Give the extent of all uninfected red blood cells.
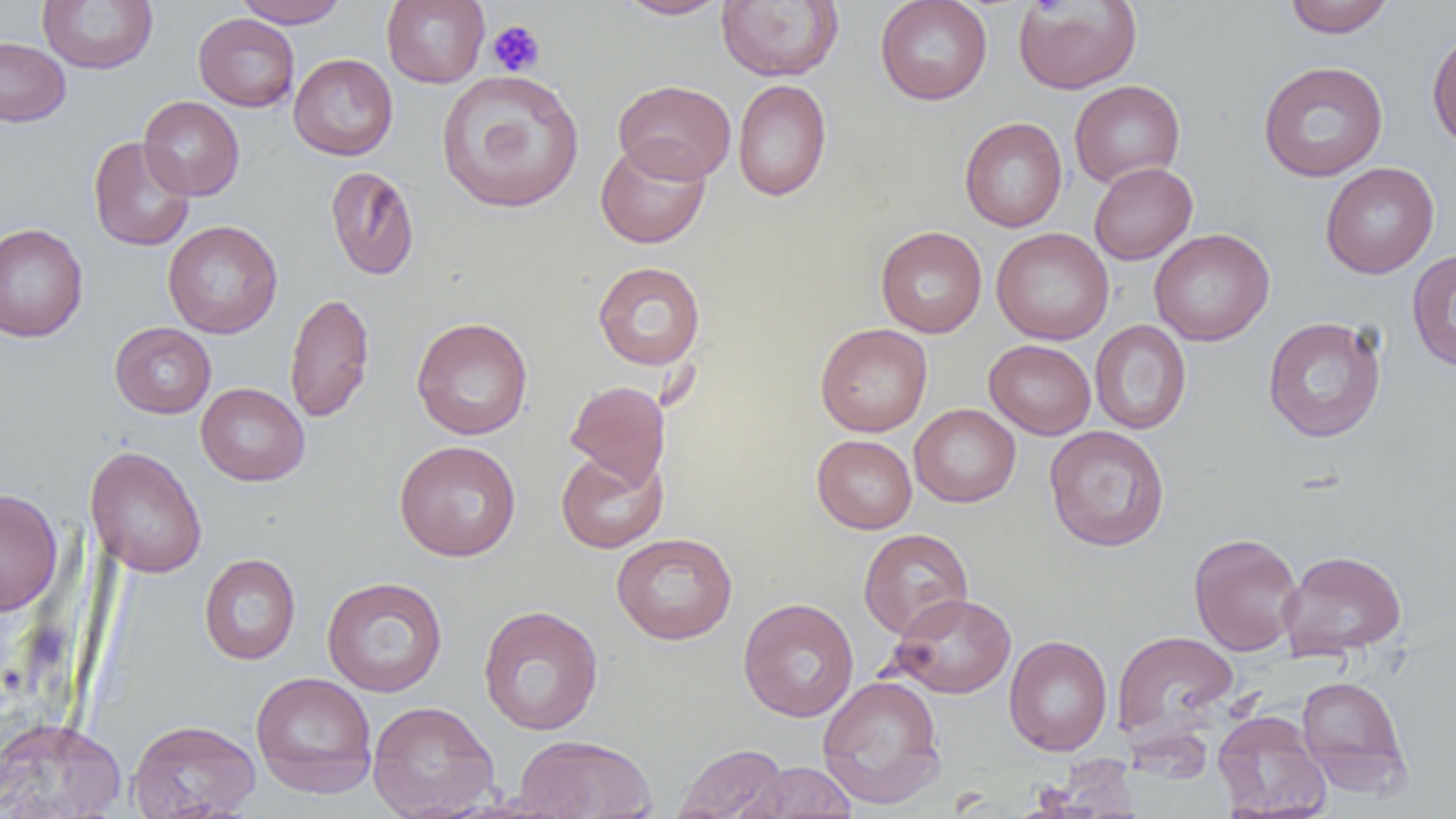

Approximate bounding boxes as [x1, y1, x2, y2] in pixels.
Uninfected red blood cells: [37, 0, 158, 74], [234, 0, 348, 28], [381, 0, 490, 88], [615, 0, 730, 20], [875, 0, 993, 105], [1283, 0, 1396, 38], [716, 1, 844, 82], [1013, 1, 1142, 94], [193, 13, 300, 112], [1427, 26, 1456, 150], [0, 35, 71, 126], [288, 53, 398, 160], [1258, 60, 1388, 182], [436, 69, 585, 214], [614, 79, 736, 184], [733, 79, 832, 201], [1069, 79, 1185, 187], [138, 96, 245, 201], [960, 117, 1067, 232], [88, 136, 195, 252], [596, 139, 711, 249], [1089, 162, 1197, 265], [1320, 162, 1439, 278], [325, 165, 420, 281], [162, 220, 283, 339], [0, 223, 88, 343], [875, 226, 987, 338], [991, 228, 1114, 345], [1150, 228, 1275, 346], [1407, 249, 1456, 373], [592, 261, 706, 370], [284, 292, 375, 423], [411, 316, 533, 440], [1262, 316, 1387, 442], [1090, 320, 1191, 435], [110, 322, 216, 419], [815, 322, 932, 436], [984, 339, 1096, 440], [565, 380, 670, 490], [196, 382, 310, 485], [909, 404, 1021, 508], [1043, 425, 1170, 551], [812, 435, 917, 533], [393, 440, 522, 561], [84, 446, 207, 578], [555, 449, 669, 554], [0, 488, 63, 616], [859, 529, 973, 640], [610, 532, 738, 645], [1188, 532, 1304, 656], [1279, 549, 1407, 660], [199, 553, 301, 665], [322, 576, 448, 697], [888, 593, 1017, 698], [738, 597, 859, 722], [478, 605, 604, 735], [1112, 630, 1238, 742], [1004, 635, 1113, 756], [250, 671, 378, 797], [817, 674, 946, 809], [1296, 675, 1412, 796], [367, 700, 499, 818], [1212, 710, 1330, 819], [0, 716, 127, 819], [127, 718, 261, 819], [511, 734, 658, 818], [674, 743, 788, 819], [1039, 756, 1144, 818], [743, 761, 857, 818].

Summary:
  - Platelet locations: [487, 20, 546, 77]
  - Slide-level diagnosis: negative for blood parasites
  - Preparation: thin blood smear
  - Magnification: 1000x
  - Field of view: one of a larger specimen
  - Modality: light microscopy
  - Image size: 1456×819 pixels